Report the malaria status of this cell.
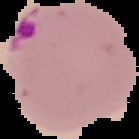

Parasitized.

Summary:
  - Image type: cell region segmented out of the field of view; surrounding area masked to black
  - Preparation: thin blood film
  - Image size: 139×139 pixels